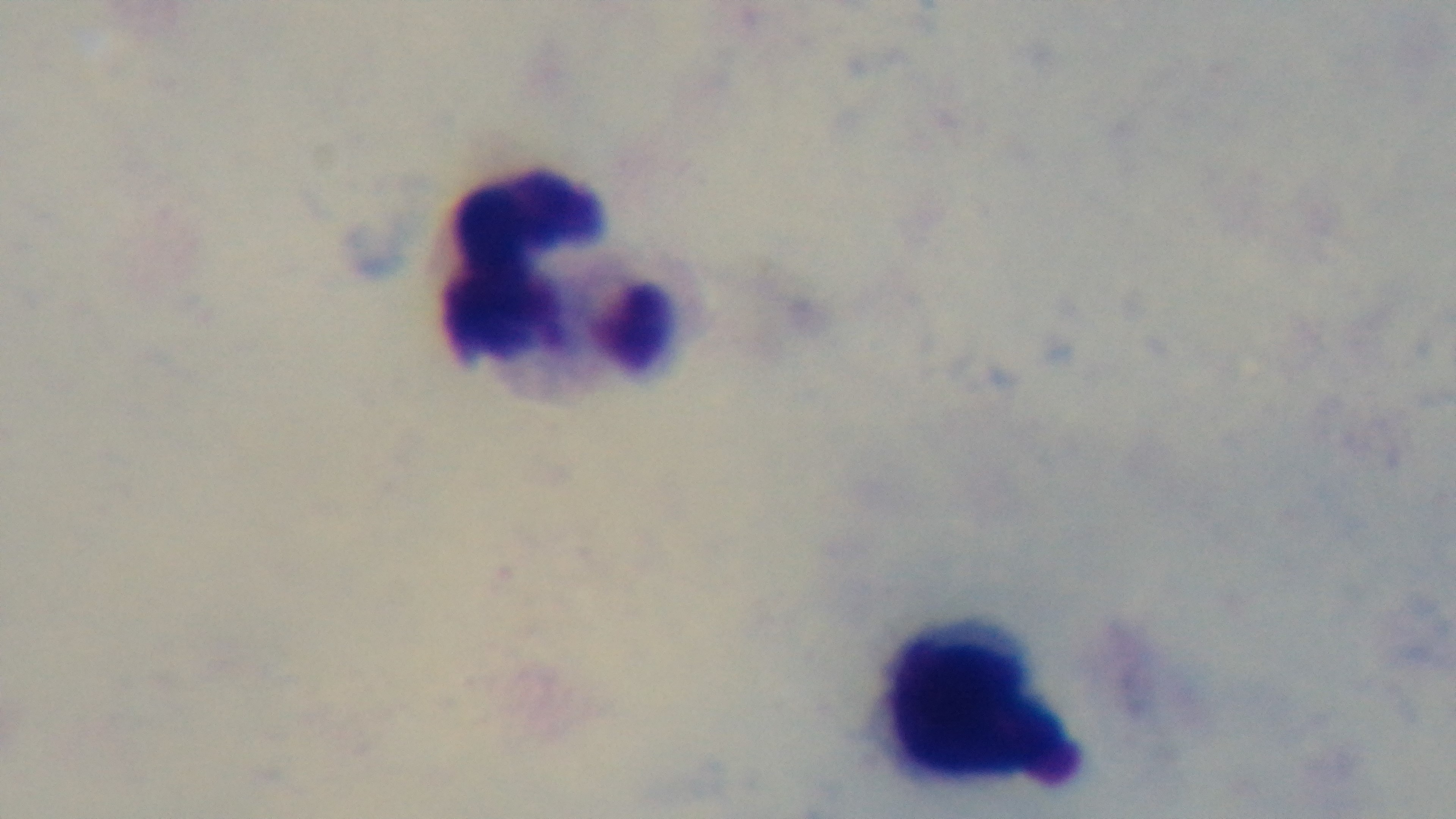

stain: Giemsa
capture: mounted 4K digital camera
field_of_view: one from the slide
preparation: thick
objective: 100x oil immersion
malaria_status: negative
modality: light microscopy